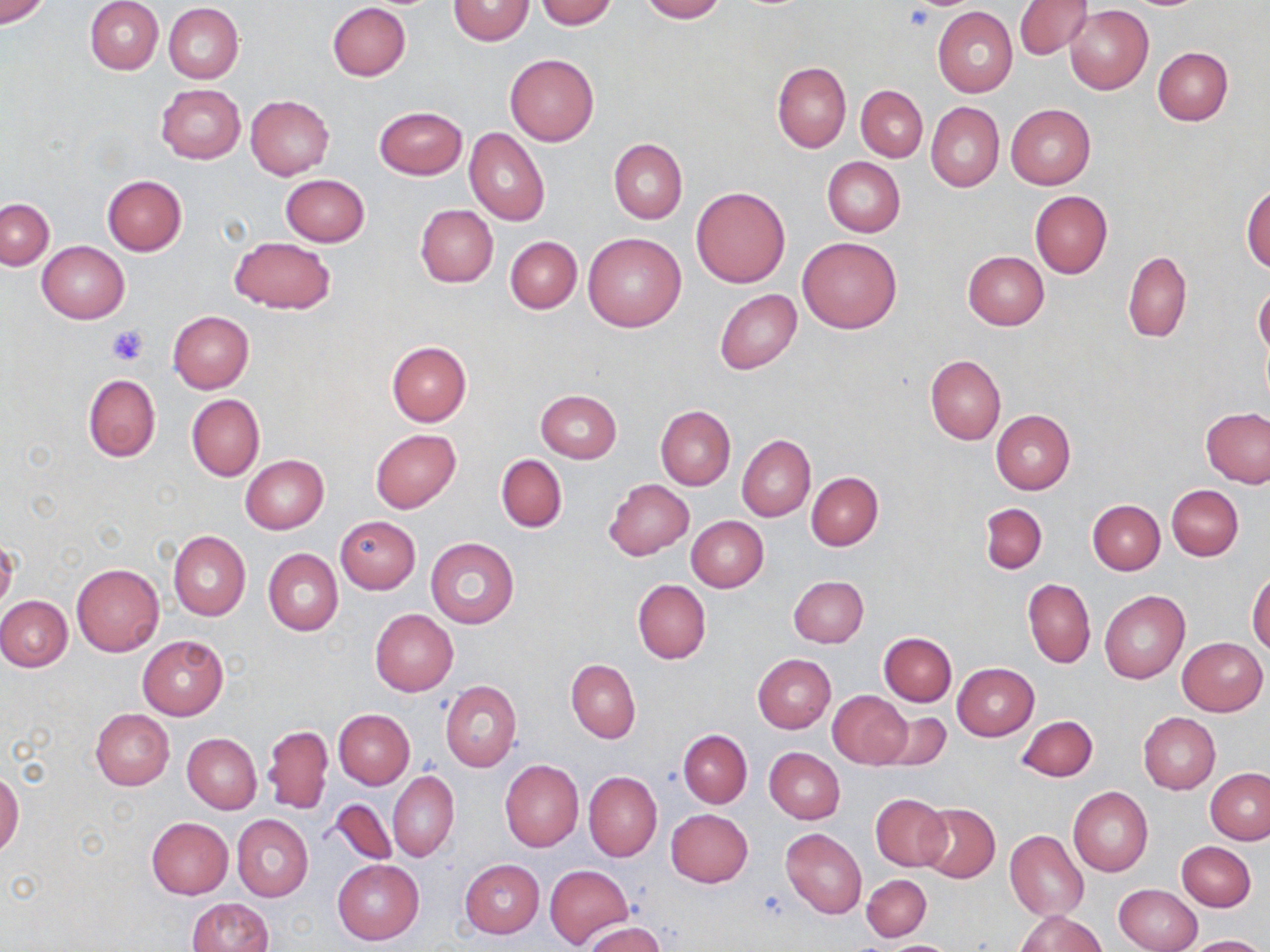

{
  "slide_level_diagnosis": "no evidence of blood parasites",
  "platelet_locations": "approximate bounding boxes as (x1,y1)-(x2,y2) corner pairs in pixels: (904,5)-(937,30), (107,325)-(149,364)",
  "uninfected_red_blood_cell_locations": "approximate bounding boxes as (x1,y1)-(x2,y2) corner pairs in pixels: (0,0)-(50,27), (84,0)-(163,75), (447,0)-(535,46), (536,0)-(616,28), (639,0)-(726,22), (1013,0)-(1090,59), (327,3)-(411,81), (162,4)-(243,84), (1065,5)-(1153,94), (932,6)-(1017,98), (1153,47)-(1232,125), (505,53)-(599,146), (773,62)-(851,152), (156,84)-(244,163), (855,85)-(928,161), (246,95)-(334,180), (925,102)-(1003,191), (1005,104)-(1094,190), (374,105)-(468,180), (465,128)-(550,225), (608,139)-(686,223), (822,156)-(905,237), (280,174)-(370,247), (103,176)-(187,255), (1242,184)-(1270,273), (690,186)-(790,288), (1030,190)-(1113,278), (1,198)-(53,269), (415,205)-(498,287), (582,233)-(686,332), (228,236)-(335,314), (506,236)-(581,313), (798,237)-(902,334), (38,242)-(129,323), (962,250)-(1049,329), (1123,251)-(1192,342), (1254,283)-(1270,359), (714,289)-(801,374), (167,311)-(253,394), (386,341)-(472,425), (925,355)-(1005,444), (82,373)-(161,461), (535,389)-(622,463), (187,394)-(264,480), (655,405)-(734,490), (1202,409)-(1270,487), (991,410)-(1076,494), (370,429)-(461,513), (737,435)-(814,521), (496,455)-(567,533), (241,456)-(329,534), (806,472)-(883,549), (604,479)-(695,560), (1167,484)-(1243,560), (1088,499)-(1164,574), (979,503)-(1047,573), (686,515)-(768,592), (336,517)-(420,594), (169,530)-(250,621), (426,537)-(519,627), (264,549)-(342,636), (71,563)-(164,656), (1247,570)-(1270,655), (789,575)-(868,647), (1023,578)-(1095,668), (633,580)-(710,664), (1100,590)-(1189,684), (0,595)-(72,671), (369,609)-(458,695), (879,633)-(956,706), (138,636)-(228,719), (1177,637)-(1268,716), (753,654)-(837,733), (567,658)-(640,744), (953,662)-(1038,740), (440,681)-(522,771), (828,690)-(911,768), (90,709)-(174,790), (334,709)-(414,790), (876,711)-(952,770), (1138,712)-(1220,793), (1016,715)-(1098,783), (262,724)-(333,813), (679,730)-(752,807), (182,734)-(261,814), (765,747)-(844,823), (500,759)-(583,851), (1205,769)-(1270,843), (0,770)-(23,857), (388,771)-(459,861), (584,771)-(662,861), (1068,786)-(1153,876), (870,793)-(949,870), (328,799)-(397,866), (919,804)-(999,883), (666,808)-(753,888), (233,814)-(313,901), (147,817)-(234,897), (780,828)-(866,918), (1005,829)-(1088,921), (1177,841)-(1255,911), (333,859)-(424,944), (460,859)-(544,938), (544,864)-(634,948), (862,874)-(931,941), (1114,883)-(1202,952), (186,898)-(273,951), (1015,910)-(1106,951), (582,922)-(665,952), (1188,934)-(1264,952), (878,940)-(963,951)",
  "image_size": "1270×952 pixels",
  "preparation": "thin blood film",
  "modality": "optical microscopy",
  "magnification": "1000x",
  "field_of_view": "one of a larger specimen",
  "stain": "May-Grünwald-Giemsa"
}